Describe the morphology of the erythrocytes.
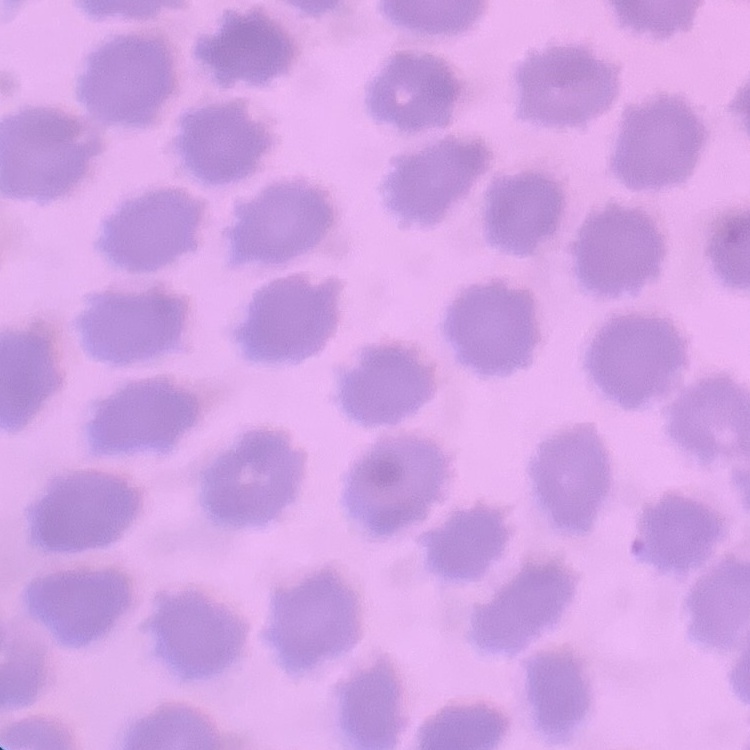
No rouleaux formation.

stain = Field's or Giemsa
preparation = thin peripheral smear
image type = square crop of a larger photomicrograph